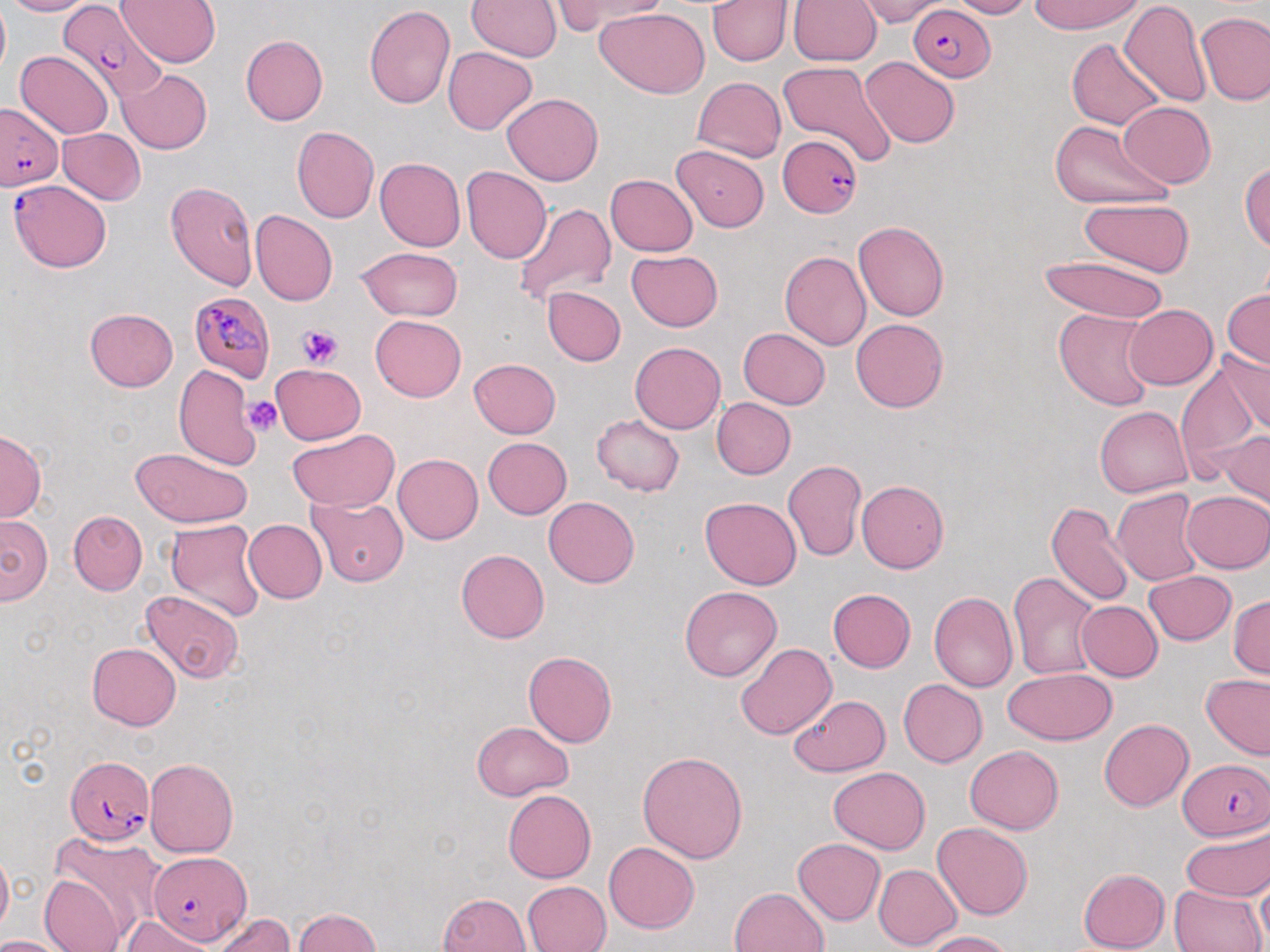
Summary:
  - Coordinate format: approximate bounding boxes as named x1/y1/x2/y2 corners in pixels
  - Plasmodium falciparum-infected red blood cell locations: (x1=56, y1=1, x2=165, y2=109), (x1=908, y1=3, x2=995, y2=82), (x1=0, y1=101, x2=64, y2=190), (x1=780, y1=136, x2=864, y2=219), (x1=9, y1=179, x2=111, y2=273), (x1=188, y1=291, x2=276, y2=383), (x1=65, y1=757, x2=154, y2=845), (x1=1181, y1=757, x2=1269, y2=841), (x1=147, y1=853, x2=251, y2=946)
  - Platelet locations: (x1=298, y1=324, x2=342, y2=368), (x1=244, y1=396, x2=283, y2=436)
  - Uninfected red blood cell locations: (x1=1, y1=0, x2=97, y2=17), (x1=117, y1=0, x2=222, y2=67), (x1=467, y1=0, x2=560, y2=61), (x1=549, y1=0, x2=673, y2=32), (x1=855, y1=0, x2=949, y2=26), (x1=947, y1=0, x2=1034, y2=19), (x1=1027, y1=0, x2=1144, y2=35), (x1=0, y1=1, x2=10, y2=81), (x1=707, y1=1, x2=790, y2=66), (x1=790, y1=1, x2=881, y2=67), (x1=1120, y1=1, x2=1212, y2=106), (x1=363, y1=4, x2=454, y2=109), (x1=595, y1=7, x2=709, y2=99), (x1=1196, y1=11, x2=1269, y2=105), (x1=240, y1=35, x2=328, y2=125), (x1=1069, y1=39, x2=1165, y2=131), (x1=442, y1=47, x2=538, y2=135), (x1=15, y1=50, x2=114, y2=138), (x1=861, y1=56, x2=960, y2=148), (x1=778, y1=61, x2=899, y2=166), (x1=118, y1=70, x2=212, y2=154), (x1=693, y1=76, x2=786, y2=162), (x1=501, y1=92, x2=603, y2=186), (x1=1119, y1=102, x2=1216, y2=188), (x1=1049, y1=120, x2=1172, y2=210), (x1=291, y1=125, x2=379, y2=224), (x1=57, y1=127, x2=146, y2=204), (x1=672, y1=145, x2=769, y2=232), (x1=375, y1=157, x2=464, y2=251), (x1=1240, y1=161, x2=1269, y2=254), (x1=461, y1=168, x2=552, y2=264), (x1=605, y1=174, x2=699, y2=256), (x1=164, y1=180, x2=258, y2=290), (x1=1079, y1=197, x2=1194, y2=277), (x1=513, y1=200, x2=618, y2=306), (x1=250, y1=210, x2=337, y2=307), (x1=852, y1=220, x2=950, y2=322), (x1=355, y1=246, x2=463, y2=322), (x1=625, y1=249, x2=724, y2=332), (x1=780, y1=251, x2=872, y2=349), (x1=1037, y1=254, x2=1170, y2=324), (x1=541, y1=287, x2=626, y2=366), (x1=1223, y1=288, x2=1269, y2=372), (x1=1122, y1=304, x2=1218, y2=389), (x1=85, y1=307, x2=178, y2=391), (x1=1053, y1=308, x2=1159, y2=412), (x1=370, y1=314, x2=466, y2=402), (x1=850, y1=318, x2=949, y2=414), (x1=738, y1=327, x2=830, y2=409), (x1=630, y1=341, x2=726, y2=434), (x1=1218, y1=343, x2=1270, y2=436), (x1=468, y1=359, x2=560, y2=439), (x1=1174, y1=359, x2=1258, y2=483), (x1=270, y1=363, x2=366, y2=445), (x1=174, y1=364, x2=263, y2=469), (x1=710, y1=398, x2=796, y2=479), (x1=1095, y1=405, x2=1192, y2=498), (x1=592, y1=414, x2=684, y2=496), (x1=0, y1=429, x2=46, y2=523), (x1=285, y1=429, x2=398, y2=512), (x1=1221, y1=431, x2=1269, y2=513), (x1=483, y1=437, x2=572, y2=518), (x1=131, y1=447, x2=254, y2=528), (x1=393, y1=453, x2=483, y2=544), (x1=783, y1=461, x2=866, y2=561), (x1=709, y1=478, x2=860, y2=576), (x1=857, y1=480, x2=949, y2=573), (x1=1112, y1=488, x2=1204, y2=586), (x1=1181, y1=491, x2=1270, y2=573), (x1=544, y1=496, x2=639, y2=587), (x1=700, y1=497, x2=800, y2=590), (x1=307, y1=499, x2=410, y2=586), (x1=1045, y1=500, x2=1135, y2=606), (x1=68, y1=510, x2=147, y2=595), (x1=0, y1=514, x2=52, y2=605), (x1=166, y1=519, x2=265, y2=622), (x1=243, y1=519, x2=327, y2=603), (x1=456, y1=549, x2=549, y2=643), (x1=1008, y1=571, x2=1101, y2=681), (x1=1143, y1=571, x2=1236, y2=645), (x1=680, y1=587, x2=782, y2=681), (x1=828, y1=588, x2=916, y2=672), (x1=139, y1=589, x2=244, y2=683), (x1=929, y1=590, x2=1018, y2=692), (x1=1229, y1=594, x2=1269, y2=679), (x1=1076, y1=600, x2=1163, y2=681), (x1=87, y1=643, x2=181, y2=730), (x1=736, y1=643, x2=836, y2=740), (x1=523, y1=651, x2=617, y2=748), (x1=1004, y1=668, x2=1115, y2=745), (x1=1201, y1=675, x2=1270, y2=760), (x1=898, y1=678, x2=987, y2=767), (x1=789, y1=694, x2=888, y2=776), (x1=1099, y1=718, x2=1193, y2=812), (x1=471, y1=721, x2=574, y2=801), (x1=964, y1=745, x2=1063, y2=834), (x1=638, y1=750, x2=749, y2=862), (x1=144, y1=758, x2=239, y2=857), (x1=828, y1=767, x2=929, y2=854), (x1=503, y1=790, x2=597, y2=883), (x1=932, y1=821, x2=1033, y2=920), (x1=1180, y1=823, x2=1270, y2=902), (x1=50, y1=830, x2=168, y2=940), (x1=791, y1=839, x2=884, y2=926), (x1=604, y1=842, x2=699, y2=933), (x1=0, y1=845, x2=13, y2=939), (x1=874, y1=864, x2=961, y2=948), (x1=1077, y1=868, x2=1170, y2=952), (x1=1255, y1=873, x2=1270, y2=946), (x1=38, y1=874, x2=128, y2=952), (x1=522, y1=881, x2=610, y2=951), (x1=1170, y1=884, x2=1265, y2=951), (x1=730, y1=886, x2=829, y2=952), (x1=437, y1=892, x2=531, y2=952), (x1=291, y1=907, x2=383, y2=952), (x1=210, y1=912, x2=296, y2=952), (x1=122, y1=915, x2=217, y2=952), (x1=927, y1=930, x2=1016, y2=952), (x1=0, y1=934, x2=74, y2=951)
  - Slide-level diagnosis: Plasmodium falciparum
  - Image size: 1270×952 pixels
  - Field of view: one of a larger specimen
  - Preparation: thin blood smear
  - Modality: light microscopy
  - Stain: May-Grünwald-Giemsa
  - Magnification: 1000x